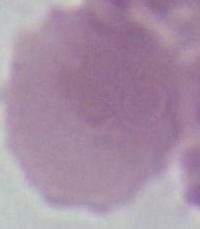

Summary:
  - Magnification: 1000x
  - Modality: micrograph
  - Identification: erythrocyte